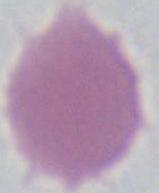
magnification: 1000x
identification: erythrocyte
modality: photomicrograph